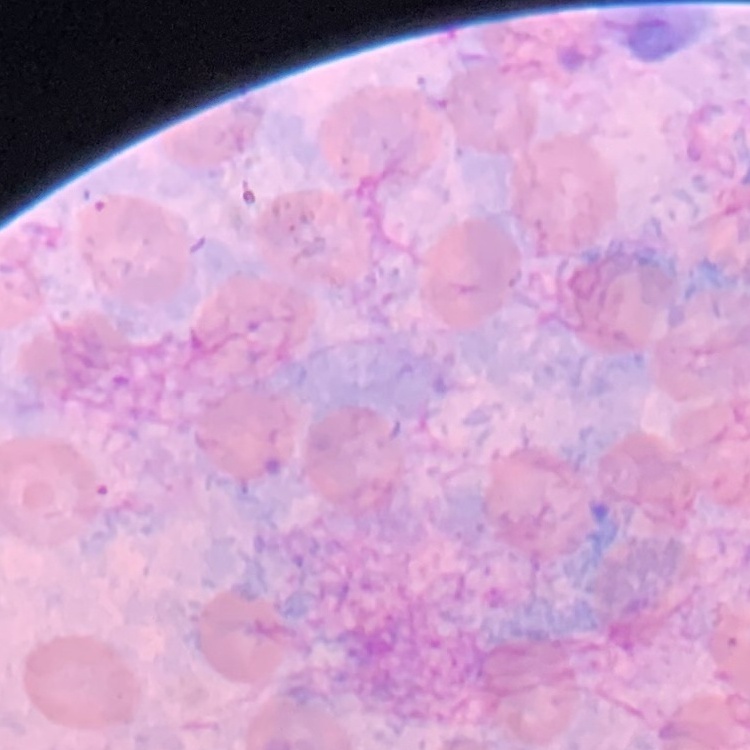
The red blood cells show no rouleaux formation. Field's or Giemsa stain. Thin blood film. Square crop of a larger photomicrograph.